Locate every malaria parasite.
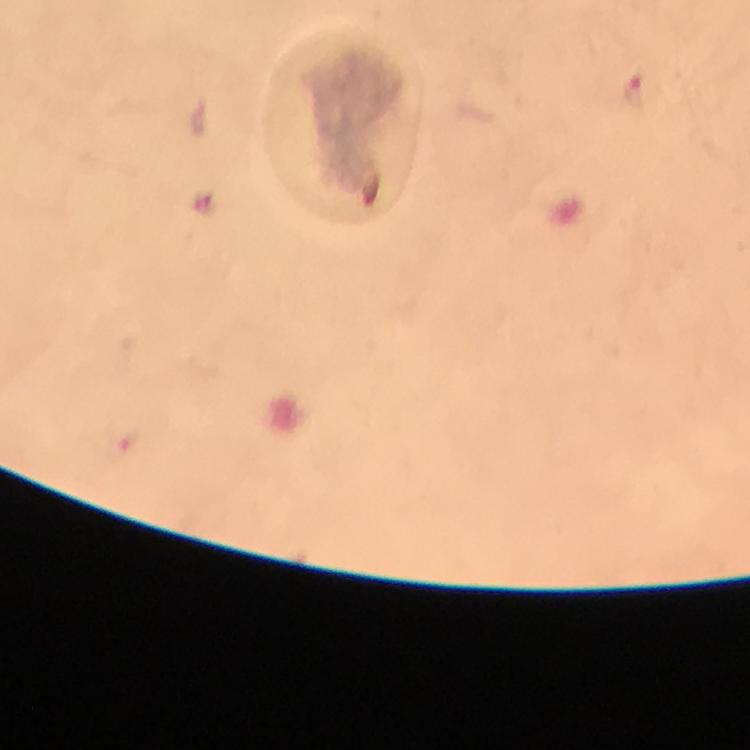
Approximate centers as {x, y} in pixels.
Malaria parasites: {637, 91}.

image size = 750×750 pixels
stain = Giemsa
preparation = thick blood film
magnification = 100x
capture = smartphone mounted on the microscope
cropped from = one field of view
context = from a diagnostic examination for malaria
immersion oil = applied